Give the position of every leukocyte visible.
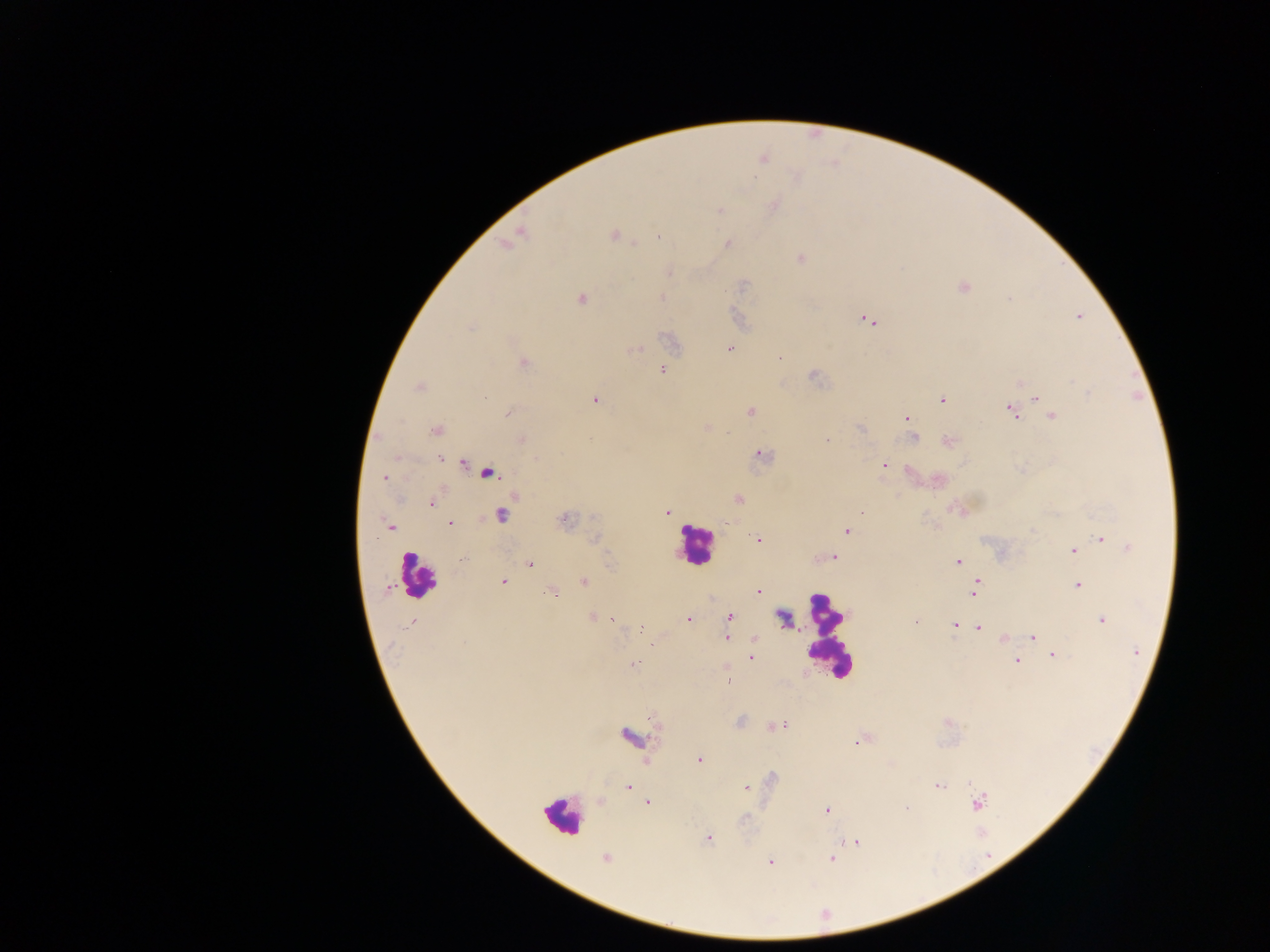

Approximate centers as (x, y) in pixels.
Leukocytes: (692, 543), (416, 573), (832, 636), (562, 815).

Summary:
  - Plasmodium parasite locations: (615, 234), (659, 235), (727, 243), (634, 245), (800, 260), (741, 286), (961, 289), (661, 296), (582, 297), (1008, 298), (861, 317), (1079, 317), (873, 322), (472, 327), (729, 348), (638, 350), (781, 357), (524, 362), (662, 369), (813, 376), (1073, 382), (418, 387), (1089, 393), (1036, 399), (596, 401), (942, 401), (1008, 408), (750, 412), (507, 414), (1053, 416), (908, 418), (706, 427), (861, 429), (436, 431), (726, 433), (913, 438), (829, 439), (946, 440), (759, 453), (765, 456), (439, 457), (462, 464), (883, 465), (487, 473), (384, 478), (514, 496), (737, 499), (433, 503), (950, 507), (861, 510), (668, 512), (500, 516), (564, 520), (450, 523), (392, 529), (846, 531), (593, 537), (756, 538), (1100, 539), (1128, 545), (1072, 550), (834, 557), (462, 559), (957, 561), (609, 562), (529, 566), (979, 580), (501, 581), (582, 582), (1076, 583), (976, 584), (388, 589), (756, 591), (552, 593), (972, 595), (591, 615), (729, 616), (787, 617), (687, 618), (1102, 619), (615, 620), (915, 621), (413, 622), (955, 623), (640, 627), (727, 629), (979, 629), (644, 631), (726, 637), (1032, 637), (1003, 638), (754, 639), (463, 643), (1053, 655), (750, 657), (1017, 661), (634, 662), (728, 683), (739, 720), (781, 725), (772, 726), (654, 733), (855, 740), (700, 758), (938, 786), (628, 787), (745, 787), (647, 802), (977, 803), (908, 807), (827, 811), (745, 818), (709, 837), (857, 842), (607, 860), (830, 860), (771, 863)
  - Field of view: single
  - Country: Ghana
  - Preparation: thick blood smear
  - Image size: 1270×952 pixels
  - Capture: mobile-phone photograph through a microscope